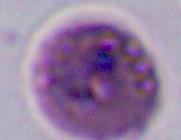
Summary:
  - Magnification: 400x or 1000x
  - Identification: Plasmodium
  - Modality: photomicrograph